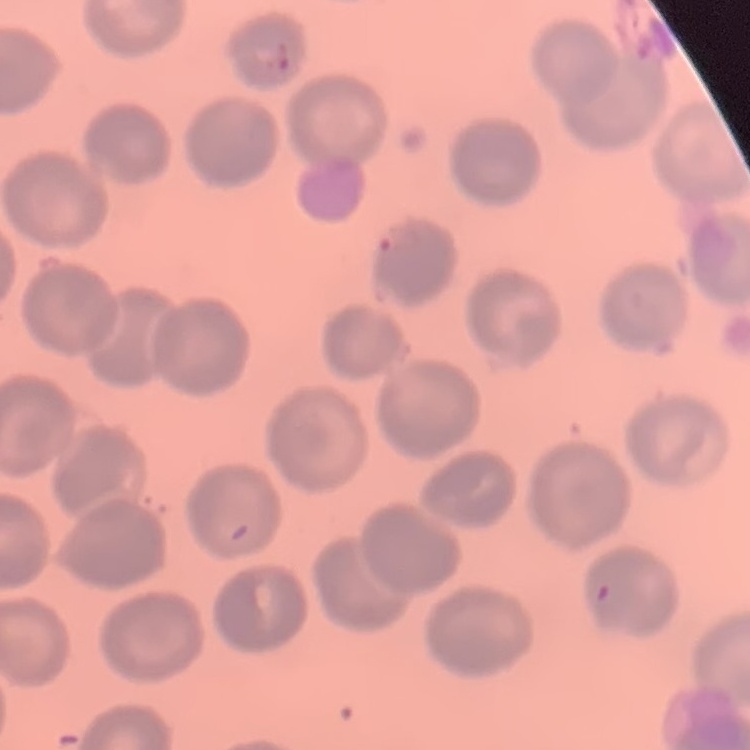

erythrocyte morphology = no rouleaux formation
image type = square crop of a larger photomicrograph
stain = Field's or Giemsa
preparation = thin blood film